Classify the preparation.
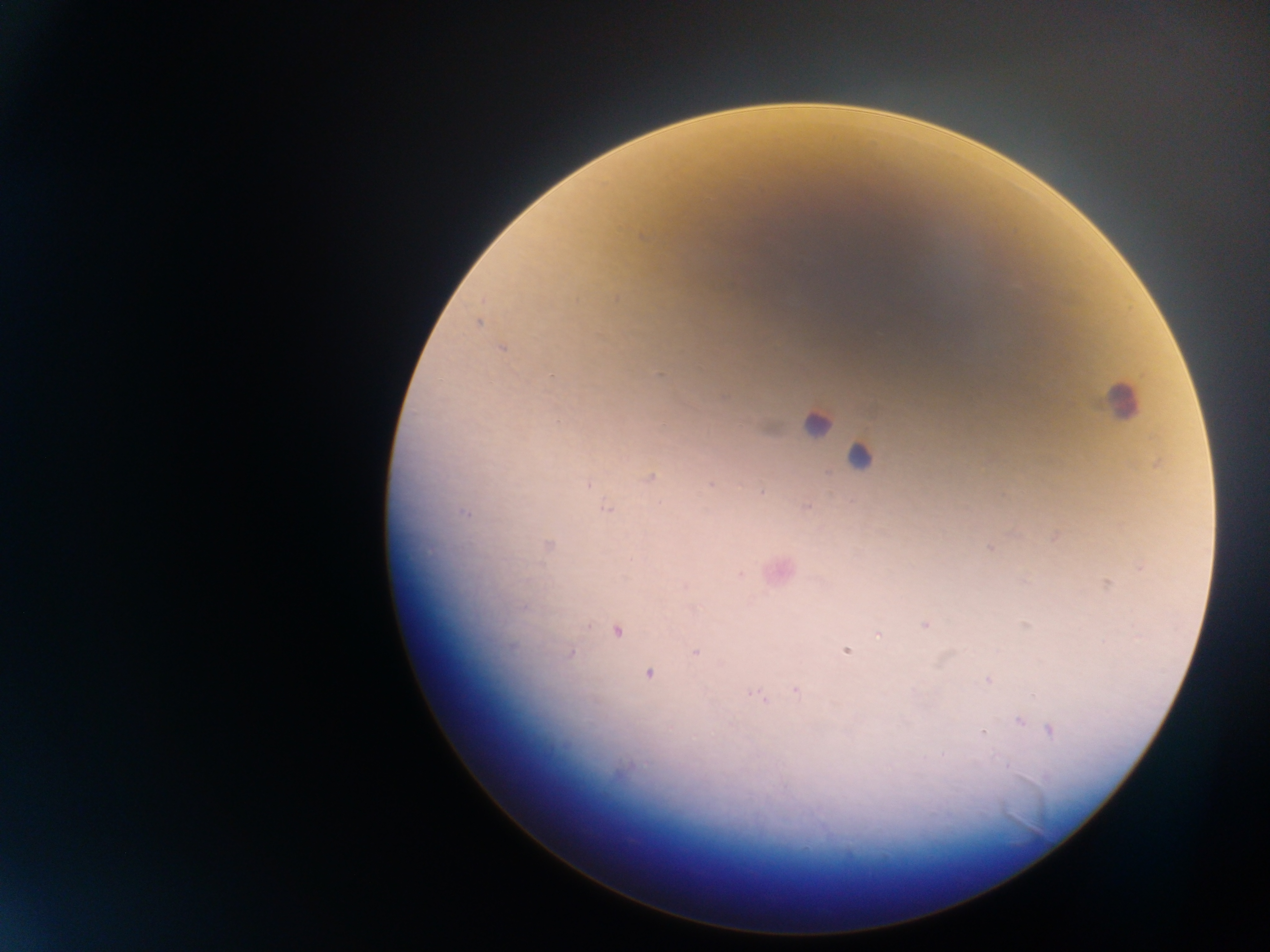
Thick blood smear.

Approximate centers as {x, y} in pixels. Leukocyte locations: {1122, 401}, {816, 424}, {860, 458}. Plasmodium parasite locations: {643, 237}, {615, 297}, {478, 323}, {501, 348}, {1158, 462}, {650, 477}, {588, 484}, {711, 484}, {762, 490}, {806, 508}, {607, 509}, {465, 513}, {549, 545}, {990, 548}, {1141, 567}, {740, 574}, {1106, 584}, {925, 625}, {1026, 626}, {617, 631}, {879, 635}, {846, 651}, {696, 652}, {570, 654}, {648, 674}, {988, 680}, {796, 690}, {759, 697}, {1020, 721}, {1051, 730}, {983, 731}, {943, 754}. Collected in Ghana. Image is 1270×952 pixels. One field of view. Photographed through a microscope with a mobile-phone camera.